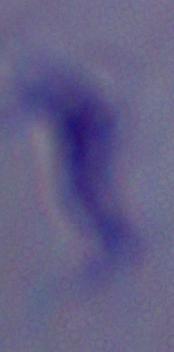
Photomicrograph. 1000x magnification. A trypanosome is shown.